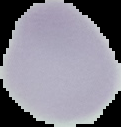

Summary:
  - Malaria status: uninfected
  - Image type: cell region segmented out of the field of view; surrounding area masked to black
  - Preparation: thin blood smear
  - Image size: 121×127 pixels